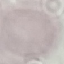
malaria_status: uninfected
image_type: automatically extracted cell patch, resized to 64 × 64 pixels
capture: smartphone through the microscope eyepiece
stain: Giemsa
preparation: thin blood film